Describe the morphology of the erythrocytes.
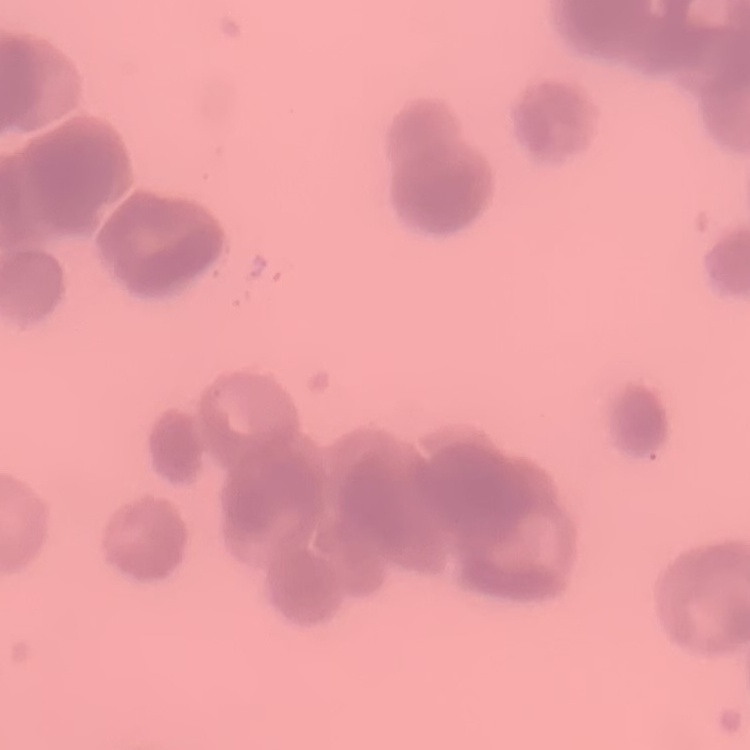

Rouleaux formation.

Stained with either Field's or Giemsa. Square crop of a larger photomicrograph. Thin peripheral smear.